Identify the blood parasite species.
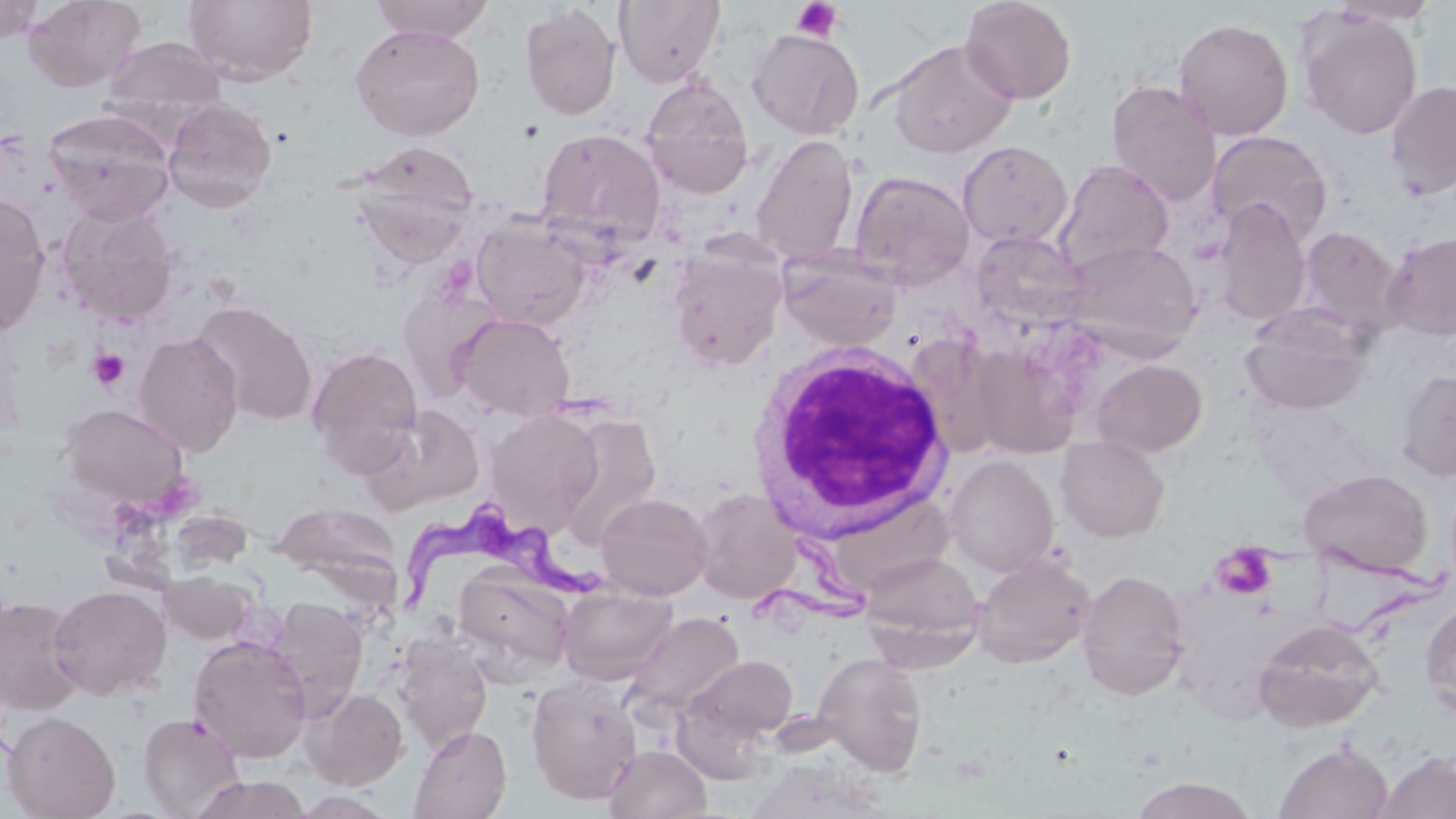
Trypanosoma brucei.

Summary:
  - Coordinate format: approximate bounding boxes as named x1/y1/x2/y2 corners in pixels
  - Trypanosoma brucei locations: (x1=401, y1=497, x2=629, y2=620)
  - Uninfected red blood cell locations: (x1=23, y1=0, x2=146, y2=91), (x1=184, y1=0, x2=318, y2=87), (x1=369, y1=0, x2=495, y2=42), (x1=614, y1=0, x2=725, y2=87), (x1=960, y1=0, x2=1077, y2=104), (x1=1329, y1=0, x2=1442, y2=28), (x1=0, y1=1, x2=46, y2=42), (x1=519, y1=3, x2=621, y2=121), (x1=1296, y1=8, x2=1423, y2=140), (x1=1173, y1=18, x2=1294, y2=140), (x1=350, y1=24, x2=486, y2=141), (x1=747, y1=28, x2=864, y2=140), (x1=101, y1=36, x2=228, y2=125), (x1=889, y1=39, x2=1017, y2=159), (x1=640, y1=77, x2=755, y2=199), (x1=1385, y1=79, x2=1456, y2=200), (x1=1106, y1=80, x2=1223, y2=207), (x1=162, y1=98, x2=278, y2=213), (x1=42, y1=109, x2=176, y2=225), (x1=536, y1=128, x2=667, y2=247), (x1=1206, y1=130, x2=1333, y2=246), (x1=750, y1=134, x2=859, y2=266), (x1=351, y1=140, x2=480, y2=254), (x1=957, y1=141, x2=1073, y2=250), (x1=1055, y1=160, x2=1175, y2=275), (x1=849, y1=170, x2=976, y2=289), (x1=0, y1=193, x2=52, y2=336), (x1=1213, y1=199, x2=1312, y2=328), (x1=56, y1=202, x2=181, y2=325), (x1=471, y1=218, x2=593, y2=331), (x1=1296, y1=225, x2=1404, y2=336), (x1=969, y1=229, x2=1089, y2=331), (x1=1382, y1=232, x2=1456, y2=342), (x1=1064, y1=239, x2=1202, y2=354), (x1=667, y1=244, x2=787, y2=373), (x1=778, y1=246, x2=903, y2=353), (x1=398, y1=281, x2=503, y2=402), (x1=191, y1=300, x2=318, y2=426), (x1=1241, y1=306, x2=1375, y2=417), (x1=452, y1=312, x2=575, y2=421), (x1=133, y1=331, x2=244, y2=457), (x1=907, y1=336, x2=1007, y2=461), (x1=969, y1=342, x2=1080, y2=459), (x1=306, y1=344, x2=424, y2=470), (x1=1091, y1=358, x2=1208, y2=457), (x1=1395, y1=369, x2=1456, y2=482), (x1=57, y1=403, x2=189, y2=507), (x1=360, y1=403, x2=485, y2=514), (x1=485, y1=408, x2=604, y2=535), (x1=556, y1=411, x2=662, y2=546), (x1=1055, y1=436, x2=1170, y2=542), (x1=945, y1=455, x2=1060, y2=576), (x1=1299, y1=468, x2=1433, y2=578), (x1=692, y1=488, x2=802, y2=604), (x1=595, y1=492, x2=712, y2=600), (x1=273, y1=502, x2=403, y2=587), (x1=860, y1=550, x2=983, y2=663), (x1=971, y1=552, x2=1096, y2=669), (x1=452, y1=566, x2=574, y2=678), (x1=1075, y1=568, x2=1190, y2=700), (x1=160, y1=571, x2=253, y2=644), (x1=49, y1=584, x2=172, y2=700), (x1=558, y1=584, x2=677, y2=686), (x1=0, y1=595, x2=86, y2=715), (x1=267, y1=597, x2=369, y2=719), (x1=1420, y1=598, x2=1456, y2=722), (x1=624, y1=611, x2=745, y2=720), (x1=1253, y1=618, x2=1385, y2=732), (x1=393, y1=632, x2=493, y2=753), (x1=188, y1=635, x2=312, y2=763), (x1=814, y1=652, x2=929, y2=776), (x1=676, y1=653, x2=799, y2=764), (x1=526, y1=677, x2=644, y2=804), (x1=302, y1=688, x2=408, y2=789), (x1=2, y1=710, x2=120, y2=819), (x1=138, y1=711, x2=245, y2=817), (x1=409, y1=725, x2=511, y2=819), (x1=1275, y1=742, x2=1392, y2=818), (x1=604, y1=743, x2=711, y2=819), (x1=1375, y1=752, x2=1456, y2=819), (x1=189, y1=774, x2=312, y2=818), (x1=1130, y1=775, x2=1258, y2=818)
  - White blood cell locations: (x1=742, y1=343, x2=953, y2=541)
  - Platelet locations: (x1=792, y1=1, x2=843, y2=42), (x1=87, y1=348, x2=131, y2=390), (x1=1210, y1=542, x2=1278, y2=600)
  - Modality: light microscopy
  - Stain: May-Grünwald-Giemsa
  - Magnification: 1000x
  - Image size: 1456×819 pixels
  - Preparation: thin blood film
  - Field of view: one of a larger specimen